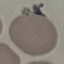

Result: negative for malaria parasites. Giemsa-stained preparation. Thin smear of blood. Photographed with a smartphone camera at the microscope eyepiece. Cell patch, automatically extracted from a larger field of view and resized to 64 × 64 pixels.